Classify this cell by malaria status.
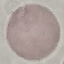

Uninfected.

Photographed with a smartphone camera at the microscope eyepiece. Giemsa-stained preparation. Thin blood smear. Cell patch, automatically extracted from a larger field of view and resized to 64 × 64 pixels.